Locate every blood parasite and identify its species.
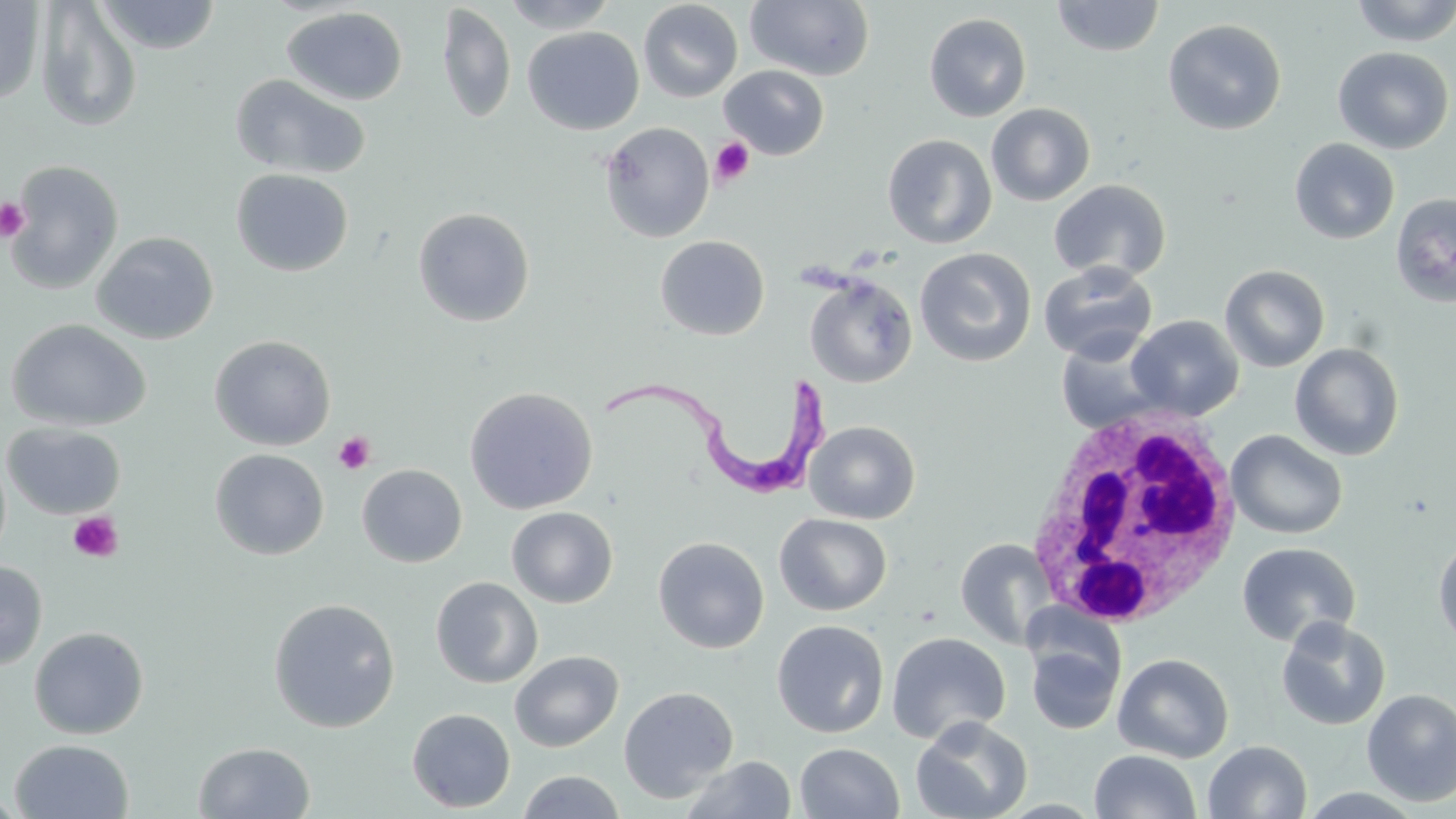

Approximate bounding boxes as (x1,y1)-(x2,y2) corner pairs in pixels.
Trypanosoma brucei: (602,365)-(839,501).
No Plasmodium falciparum, Plasmodium ovale, Plasmodium malariae, Plasmodium vivax, or Babesia divergens observed.

Uninfected red blood cell locations: (96,0)-(221,54), (499,0)-(619,33), (744,0)-(876,82), (1050,0)-(1166,58), (1350,0)-(1455,47), (0,1)-(45,106), (35,1)-(142,133), (638,1)-(743,103), (436,3)-(516,125), (281,7)-(408,106), (923,12)-(1033,122), (1163,19)-(1287,135), (523,26)-(644,135), (1332,46)-(1454,154), (719,65)-(830,160), (230,74)-(371,180), (986,103)-(1096,206), (599,122)-(715,243), (882,133)-(997,249), (1289,138)-(1400,244), (4,160)-(124,295), (231,168)-(354,277), (1048,179)-(1171,282), (1391,192)-(1456,308), (413,207)-(535,327), (91,231)-(219,345), (655,235)-(770,341), (914,247)-(1037,367), (1038,262)-(1158,363), (1220,264)-(1330,372), (805,266)-(1035,378), (804,273)-(917,387), (1126,315)-(1244,420), (6,319)-(152,432), (1055,333)-(1169,434), (209,335)-(336,451), (1290,342)-(1405,461), (463,386)-(598,514), (805,420)-(921,524), (2,422)-(126,519), (1226,429)-(1348,540), (0,447)-(11,566), (209,449)-(329,560), (357,464)-(467,567), (506,506)-(618,608), (775,513)-(892,616), (1432,533)-(1456,652), (653,536)-(770,654), (955,537)-(1058,651), (1236,542)-(1361,647), (0,560)-(48,670), (430,577)-(543,688), (268,597)-(401,732), (1275,617)-(1392,730), (771,620)-(889,738), (29,626)-(149,739), (886,632)-(1011,744), (1024,632)-(1125,737), (510,650)-(624,752), (1112,653)-(1234,763), (618,686)-(739,803), (1361,688)-(1456,807), (407,708)-(516,813), (910,716)-(1033,819), (9,739)-(134,818), (1203,740)-(1312,818), (193,742)-(316,818), (795,742)-(904,819), (1089,750)-(1201,819), (679,756)-(797,818), (517,770)-(627,819), (1296,787)-(1429,818), (0,789)-(26,818). White blood cell locations: (1023,405)-(1247,629). Platelet locations: (709,137)-(755,187), (0,197)-(28,241), (332,431)-(375,475), (66,511)-(123,563). Slide-level diagnosis: Trypanosoma brucei. Thin blood smear. Image is 1456×819 pixels. Optical microscopy. One field of a larger specimen. May-Grünwald-Giemsa-stained preparation. 1000x magnification.